State which parasite is depicted.
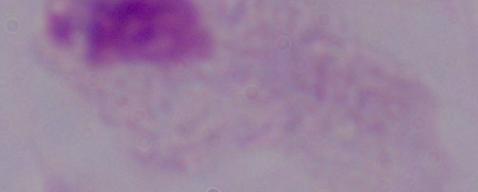
A trichomonad.

Micrograph. 1000x magnification.